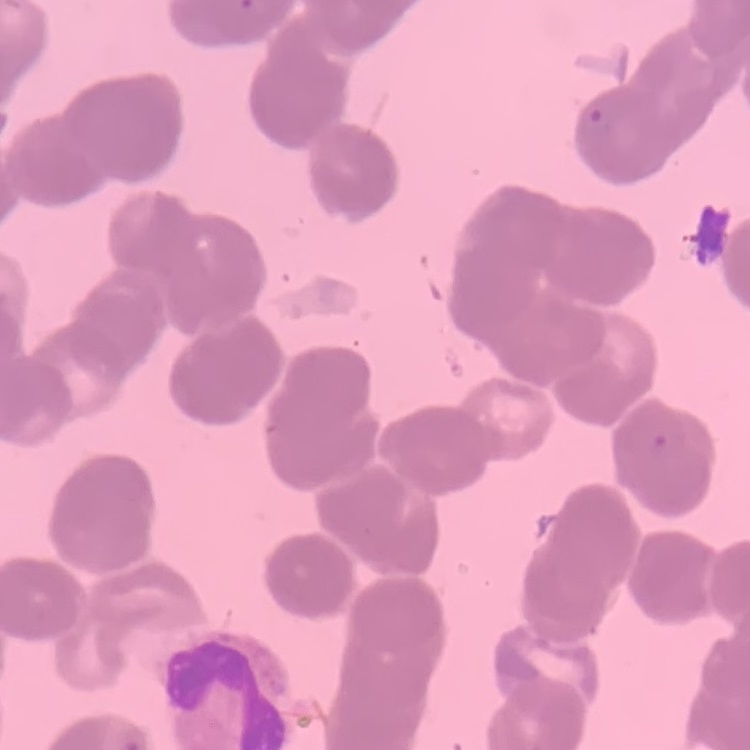 The erythrocytes exhibit rouleaux formation. Field's or Giemsa stain. Thin blood film. Square crop of a larger photomicrograph.